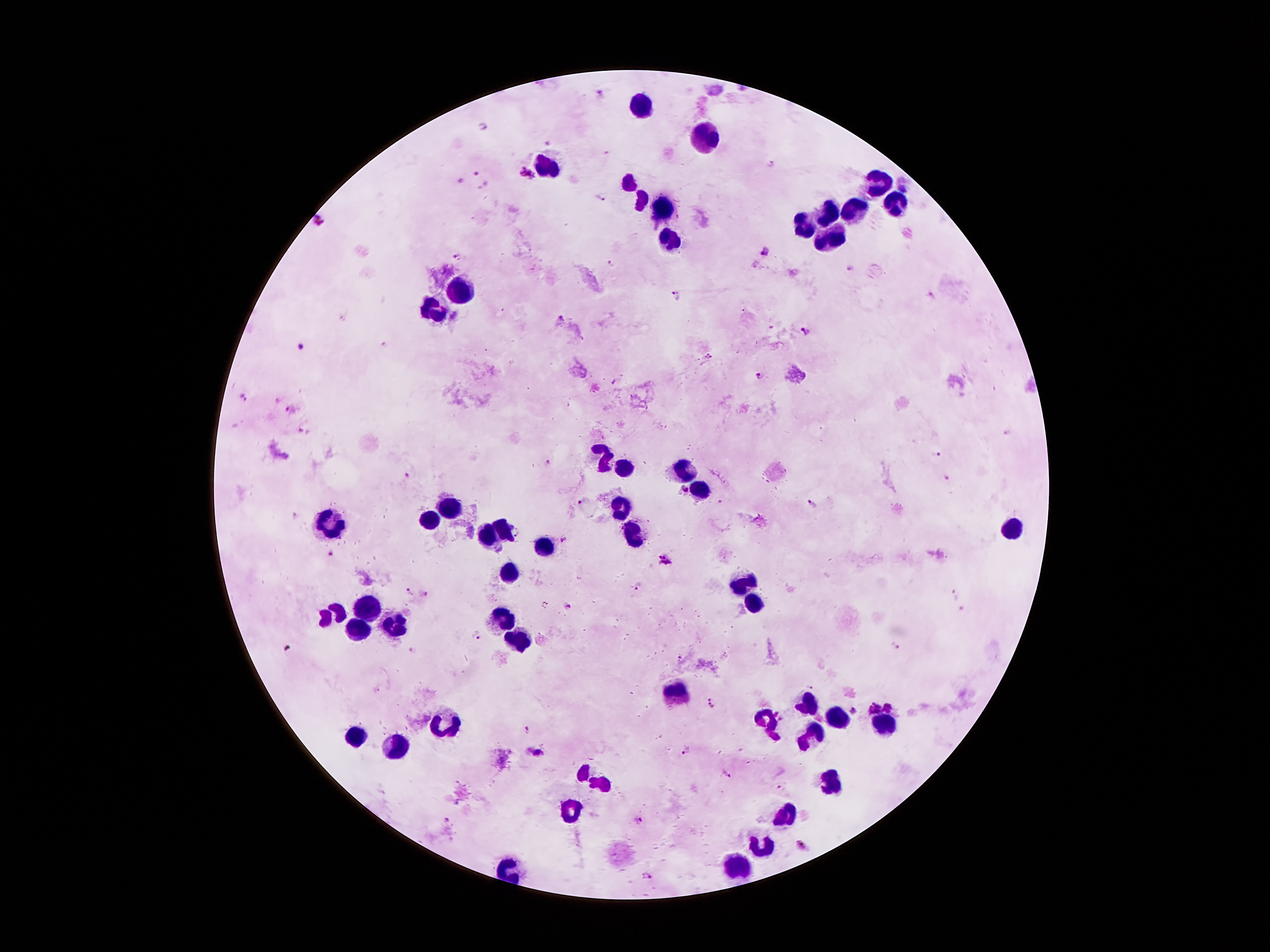

coordinate format = approximate centers as {x, y} in pixels
leukocyte locations = {640, 105}, {705, 138}, {549, 170}, {629, 182}, {876, 182}, {641, 201}, {891, 205}, {661, 209}, {855, 211}, {828, 214}, {805, 229}, {829, 237}, {669, 239}, {465, 290}, {437, 310}, {607, 455}, {681, 469}, {624, 470}, {701, 486}, {621, 509}, {449, 510}, {431, 523}, {335, 525}, {504, 527}, {1012, 530}, {632, 535}, {485, 538}, {543, 546}, {512, 575}, {741, 582}, {756, 606}, {363, 607}, {333, 615}, {396, 619}, {505, 619}, {361, 627}, {517, 639}, {676, 695}, {805, 706}, {835, 718}, {771, 725}, {443, 726}, {887, 726}, {811, 735}, {355, 738}, {397, 750}, {592, 781}, {828, 781}, {573, 811}, {785, 817}, {761, 847}, {740, 866}
malaria parasite locations = {600, 93}, {483, 127}, {548, 144}, {607, 153}, {770, 164}, {475, 173}, {526, 176}, {458, 180}, {904, 188}, {601, 197}, {319, 221}, {764, 251}, {456, 258}, {610, 264}, {853, 268}, {677, 294}, {933, 294}, {561, 317}, {806, 331}, {384, 343}, {302, 346}, {706, 356}, {757, 375}, {614, 381}, {243, 397}, {288, 409}, {1008, 434}, {938, 453}, {547, 461}, {407, 475}, {946, 479}, {683, 491}, {578, 501}, {812, 503}, {296, 516}, {564, 539}, {329, 552}, {665, 560}, {636, 583}, {407, 592}, {424, 594}, {954, 595}, {569, 606}, {960, 606}, {477, 636}, {896, 648}, {289, 649}, {414, 650}, {681, 658}, {810, 688}, {711, 704}, {871, 706}, {887, 706}, {852, 710}, {775, 712}, {782, 718}, {527, 731}, {686, 749}, {538, 753}, {725, 772}, {457, 802}, {445, 819}, {640, 820}, {802, 845}, {650, 878}
capture = smartphone through the microscope eyepiece
preparation = thick blood smear
patient malaria status = infected with Plasmodium falciparum
field of view = single
magnification = 100x
stain = Giemsa
image size = 1270×952 pixels